Assess this cell for malaria.
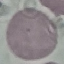
Uninfected.

{
  "stain": "Giemsa",
  "preparation": "thin blood smear",
  "image_type": "automatically extracted cell patch, resized to 64 × 64 pixels",
  "capture": "smartphone through the microscope eyepiece"
}